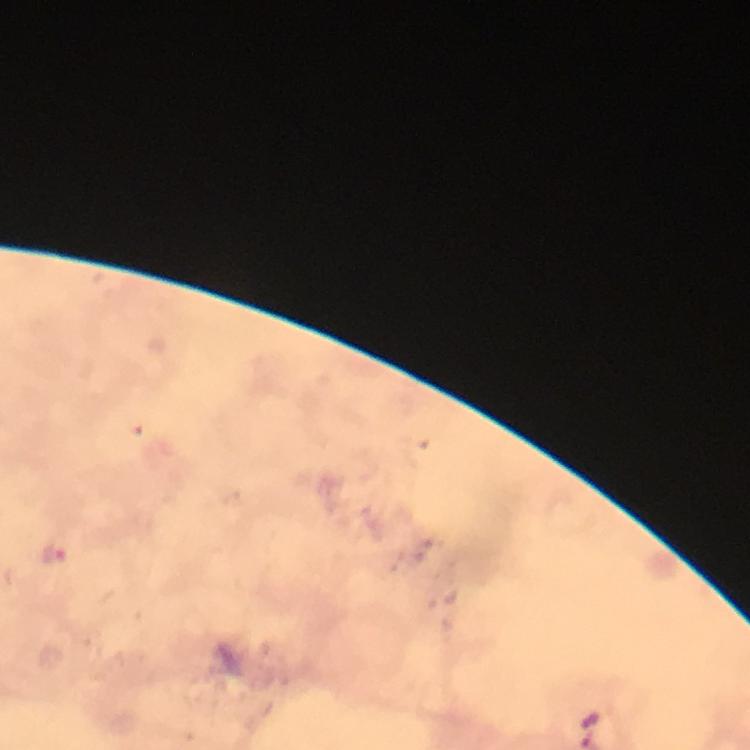
cropped from = a single field of view
capture = smartphone photograph through a microscope
stain = Giemsa
immersion oil = used
preparation = thick blood smear
malaria parasite locations = approximate centers as [x, y] in pixels: [53, 550]
context = from a diagnostic examination for malaria
image size = 750×750 pixels
magnification = 100x